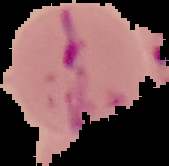

Summary:
  - Image size: 169×166 pixels
  - Image type: segmented cell region on a black background
  - Result: malaria parasites identified
  - Preparation: thin blood smear